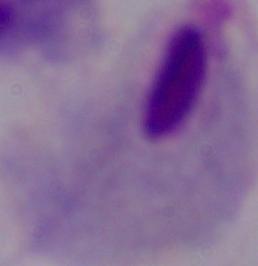
{
  "magnification": "1000x",
  "identification": "trichomonad",
  "modality": "photomicrograph"
}